Report the malaria status of this cell.
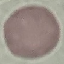
It is uninfected.

Summary:
  - Image type: cell patch, automatically extracted from a larger field of view and resized to 64 × 64 pixels
  - Preparation: thin smear
  - Capture: smartphone camera at the microscope eyepiece
  - Stain: Giemsa